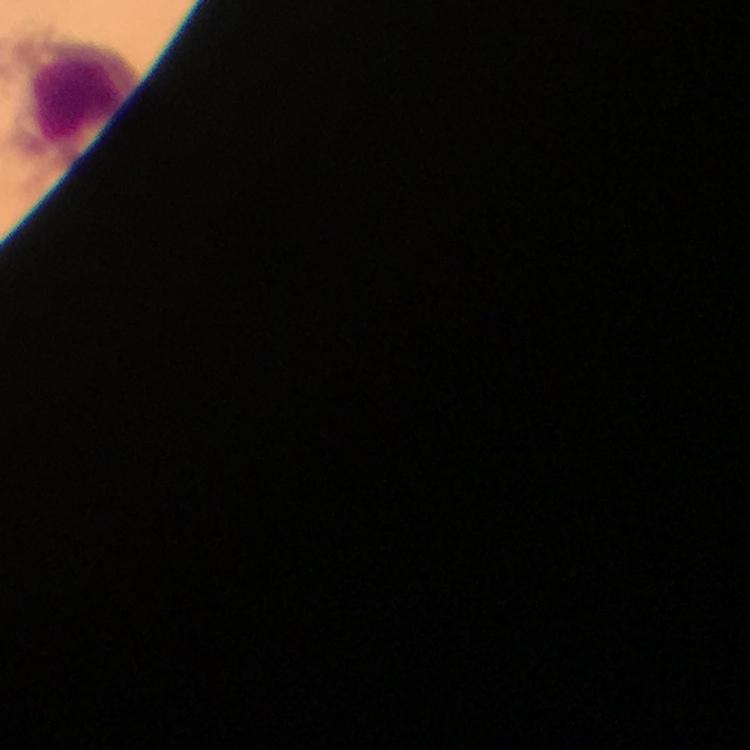
Approximate centers as [x, y] in pixels. Leukocyte locations: [79, 89]. From a diagnostic examination for malaria. Photographed with a smartphone mounted on the microscope. Image is 750×750 pixels. 100x magnification. Plasmodium parasites: none detected. Giemsa-stained preparation. Immersion oil was used. A crop from one field of view. Thick blood film.